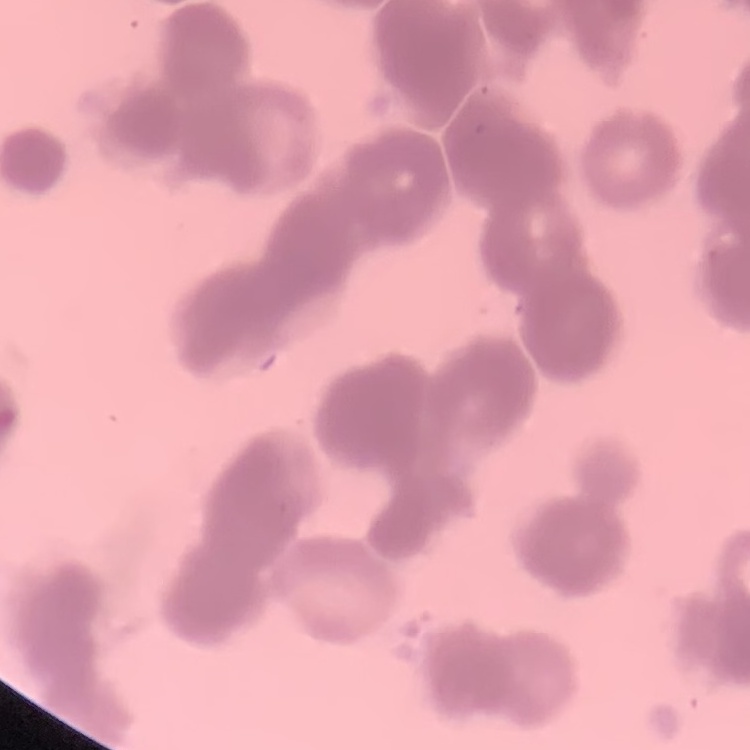
Summary:
  - Erythrocyte morphology: rouleaux formation
  - Stain: Field's or Giemsa
  - Image type: one tile cut from a larger photomicrograph
  - Preparation: thin blood film